Name the parasite shown.
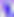

Toxoplasma gondii.

Summary:
  - Modality: micrograph
  - Magnification: 400x